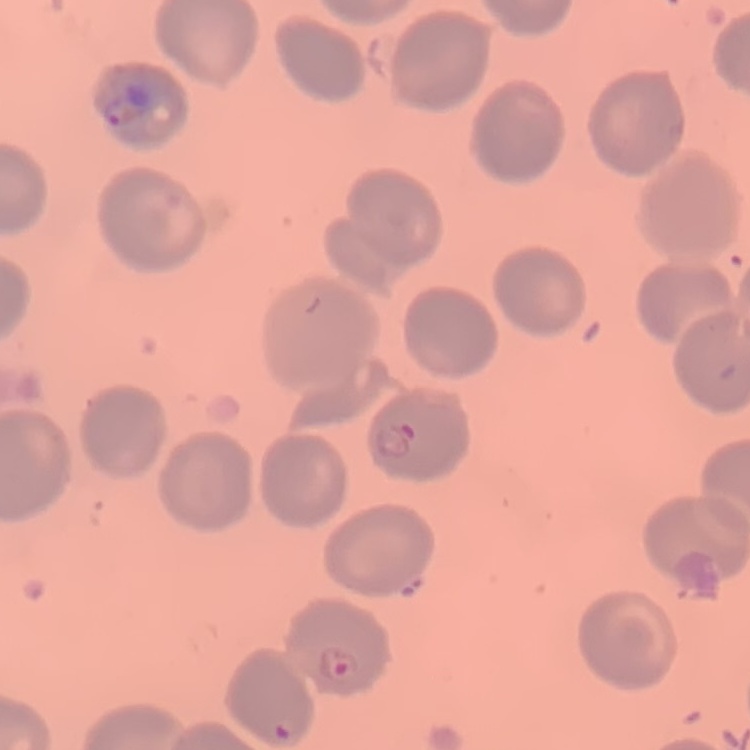

red blood cell morphology = no rouleaux formation
stain = Field's or Giemsa
image type = square crop of a larger photomicrograph
preparation = thin blood smear